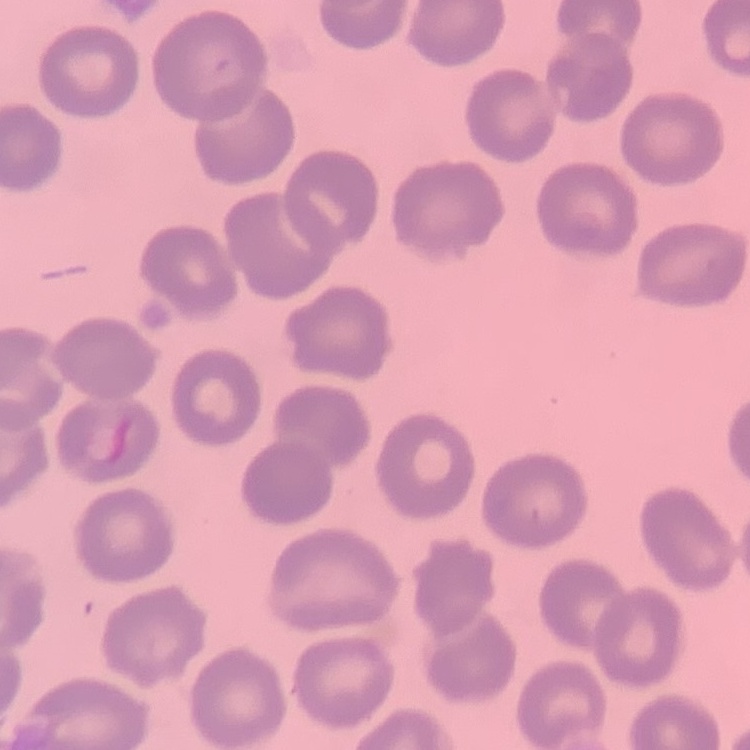

The erythrocytes exhibit no rouleaux formation. One tile cut from a larger photomicrograph. Stained with either Field's or Giemsa. Thin peripheral smear.